Assess this cell for malaria.
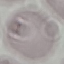
It is uninfected.

{
  "stain": "Giemsa",
  "capture": "smartphone through the microscope eyepiece",
  "image_type": "cell patch, automatically extracted from a larger field of view and resized to 64 × 64 pixels",
  "preparation": "thin blood smear"
}